Assess this cell for malaria.
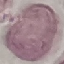
Uninfected.

{
  "capture": "smartphone camera at the microscope eyepiece",
  "image_type": "automatically extracted cell patch, resized to 64 × 64 pixels",
  "stain": "Giemsa",
  "preparation": "thin blood smear"
}